Assess this cell for malaria.
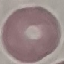
It is uninfected.

Summary:
  - Image type: automatically extracted cell patch, resized to 64 × 64 pixels
  - Preparation: thin blood smear
  - Capture: smartphone through the microscope eyepiece
  - Stain: Giemsa